Classify this cell by malaria status.
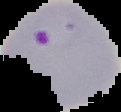

It is parasitized.

Summary:
  - Image type: segmented cell region with the area outside set to black
  - Image size: 121×112 pixels
  - Preparation: thin blood smear